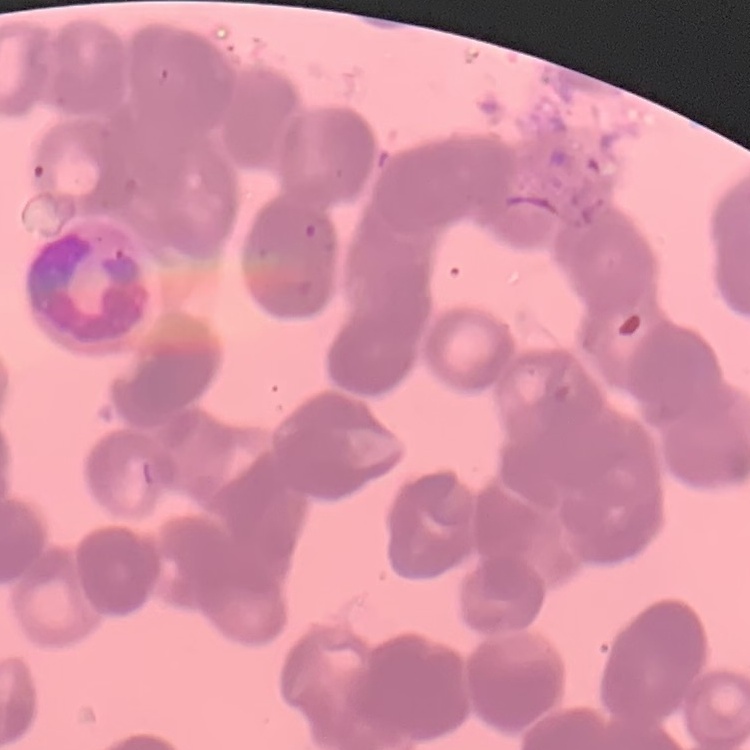
The erythrocytes show rouleaux formation. Square crop of a larger photomicrograph. Thin peripheral smear. Field's or Giemsa stain.